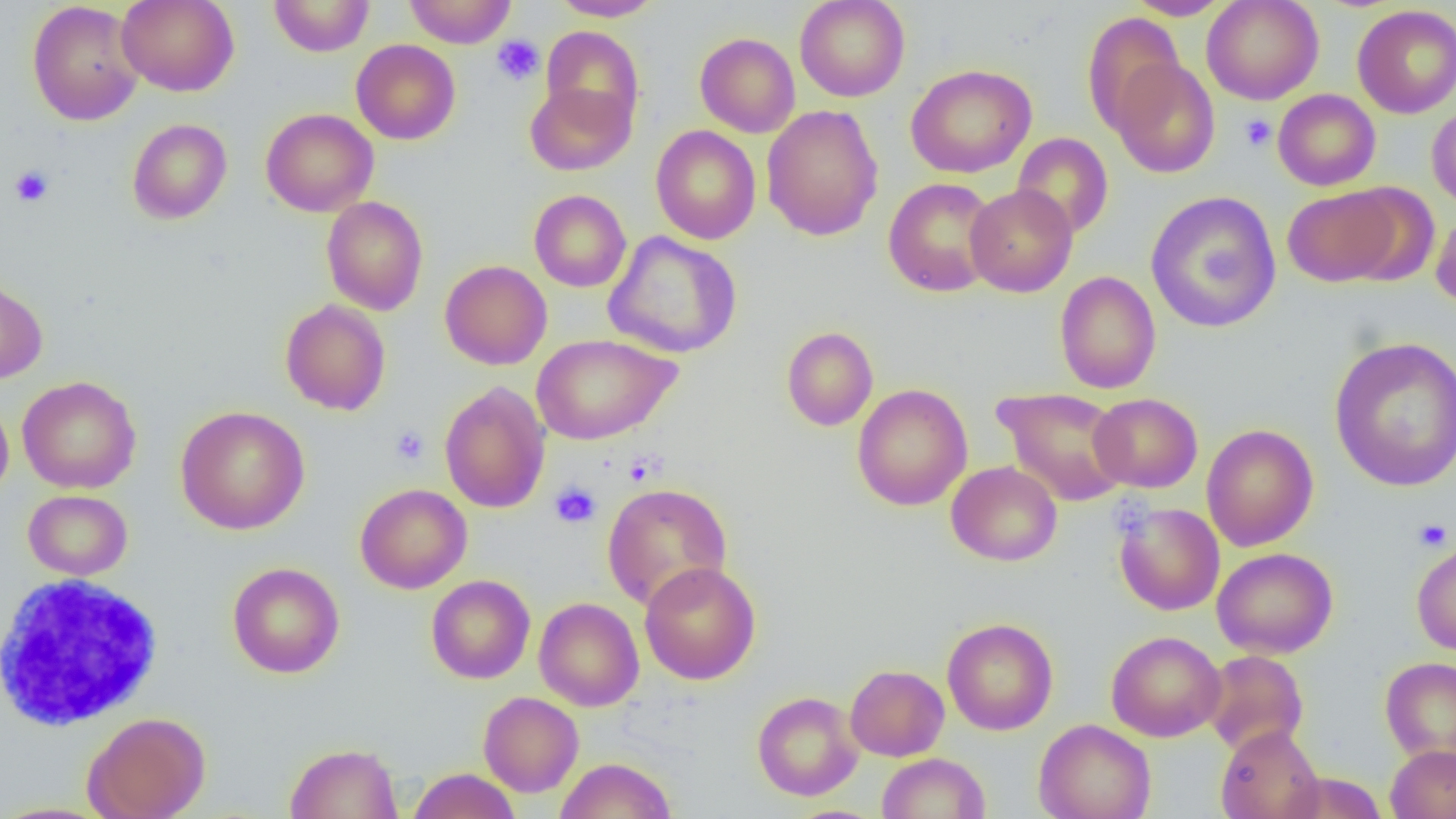

Summary:
  - Coordinate format: approximate bounding boxes as (x1, y1, x2, y2) in pixels
  - Uninfected red blood cell locations: (117, 0, 239, 96), (268, 0, 375, 57), (403, 0, 517, 48), (549, 0, 664, 21), (795, 0, 910, 102), (1125, 0, 1230, 20), (1201, 0, 1324, 104), (26, 1, 144, 126), (1352, 5, 1456, 118), (1082, 12, 1187, 135), (541, 26, 644, 131), (695, 33, 800, 138), (351, 39, 461, 145), (1108, 57, 1221, 178), (905, 63, 1037, 178), (525, 81, 635, 175), (1272, 89, 1380, 191), (761, 104, 884, 241), (1427, 104, 1456, 210), (260, 108, 378, 217), (127, 119, 232, 224), (651, 125, 761, 244), (1011, 133, 1114, 239), (883, 177, 1000, 297), (965, 184, 1077, 297), (1339, 185, 1439, 287), (1283, 186, 1403, 287), (529, 190, 631, 292), (1146, 191, 1282, 333), (321, 196, 429, 315), (1431, 210, 1456, 312), (602, 231, 742, 358), (440, 260, 552, 370), (1055, 271, 1161, 394), (0, 274, 48, 384), (280, 299, 391, 416), (781, 326, 878, 431), (531, 334, 681, 445), (1328, 335, 1456, 493), (16, 375, 142, 493), (439, 381, 551, 514), (852, 384, 973, 510), (995, 387, 1130, 506), (1089, 393, 1203, 493), (0, 394, 14, 503), (175, 405, 310, 534), (1201, 424, 1318, 551), (946, 461, 1062, 566), (602, 482, 732, 611), (355, 483, 472, 594), (23, 490, 133, 580), (1114, 502, 1225, 616), (1411, 539, 1456, 656), (1212, 547, 1338, 659), (639, 561, 761, 685), (227, 562, 344, 678), (426, 575, 535, 684), (426, 592, 642, 697), (533, 597, 644, 711), (942, 617, 1058, 735), (1106, 630, 1226, 742), (1201, 650, 1309, 756), (1379, 656, 1456, 765), (845, 664, 949, 761), (752, 691, 864, 801), (478, 692, 584, 797), (83, 711, 211, 819), (1034, 718, 1157, 819), (1215, 724, 1325, 819), (284, 742, 403, 819), (1385, 744, 1456, 819), (877, 752, 991, 818), (555, 757, 677, 819), (407, 768, 521, 819), (1284, 771, 1388, 818), (0, 801, 118, 818)
  - Platelet locations: (491, 35, 544, 86), (1239, 114, 1277, 152), (10, 165, 54, 207), (390, 425, 430, 466), (624, 452, 663, 486), (549, 482, 602, 528), (1413, 518, 1452, 551)
  - White blood cell locations: (0, 574, 165, 732)
  - Slide-level diagnosis: negative for blood parasites
  - Image size: 1456×819 pixels
  - Field of view: one of a larger specimen
  - Preparation: thin blood smear
  - Magnification: 1000x
  - Modality: light microscopy